Locate and identify every blood parasite.
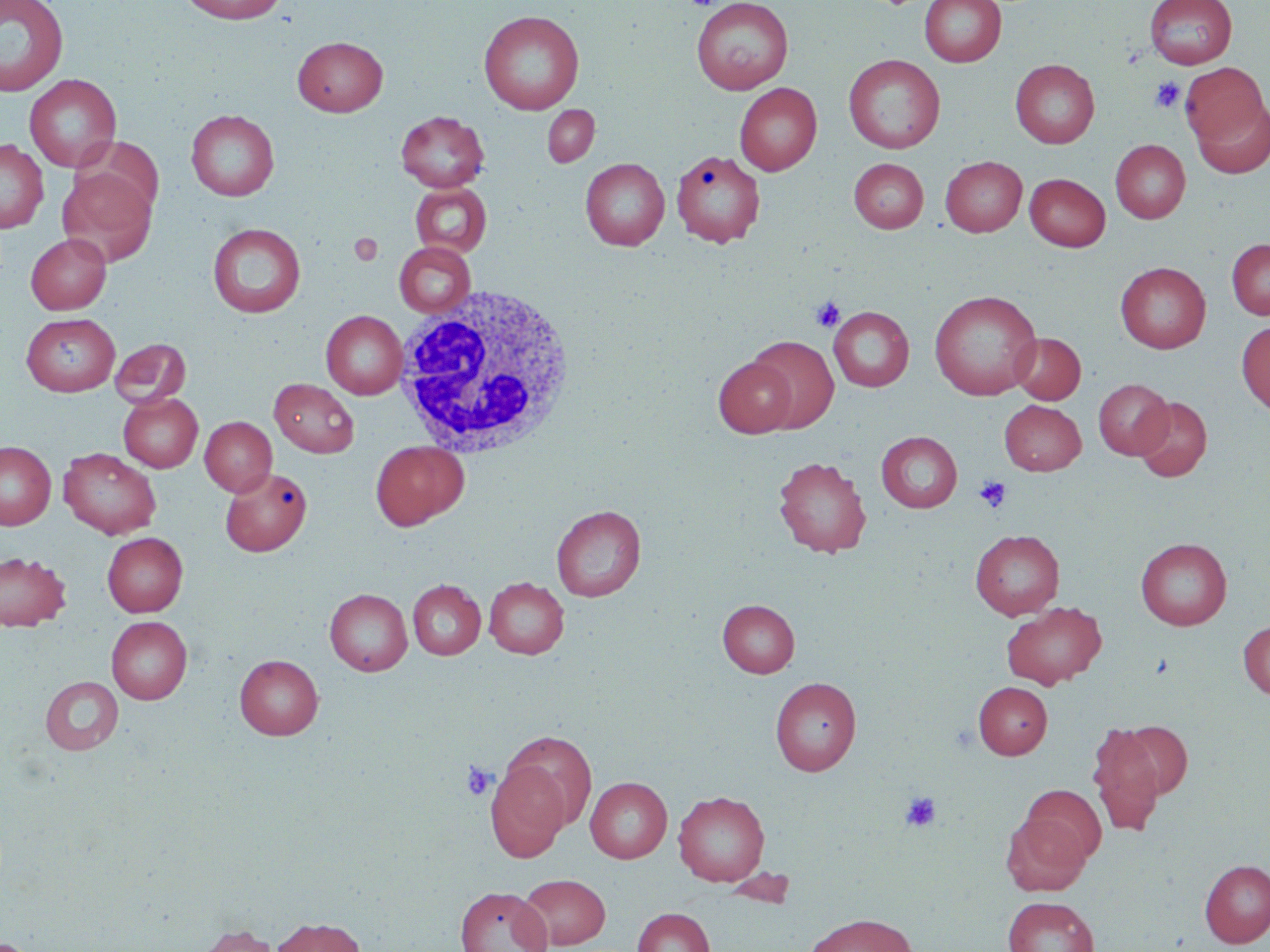

No blood parasites observed.

Approximate bounding boxes as named x1/y1/x2/y2 corners in pixels. White blood cell locations: (x1=389, y1=285, x2=580, y2=461). Uninfected red blood cell locations: (x1=0, y1=0, x2=69, y2=97), (x1=177, y1=0, x2=289, y2=24), (x1=691, y1=0, x2=793, y2=94), (x1=920, y1=0, x2=1006, y2=67), (x1=1145, y1=0, x2=1237, y2=69), (x1=479, y1=10, x2=585, y2=114), (x1=293, y1=36, x2=387, y2=116), (x1=844, y1=54, x2=945, y2=153), (x1=1010, y1=59, x2=1099, y2=148), (x1=1180, y1=63, x2=1268, y2=147), (x1=24, y1=74, x2=122, y2=173), (x1=735, y1=83, x2=822, y2=175), (x1=1191, y1=98, x2=1270, y2=178), (x1=542, y1=105, x2=599, y2=168), (x1=186, y1=109, x2=279, y2=200), (x1=396, y1=111, x2=489, y2=191), (x1=77, y1=137, x2=164, y2=218), (x1=0, y1=139, x2=49, y2=233), (x1=1110, y1=140, x2=1190, y2=223), (x1=671, y1=150, x2=765, y2=247), (x1=941, y1=156, x2=1026, y2=236), (x1=580, y1=158, x2=669, y2=251), (x1=849, y1=158, x2=928, y2=233), (x1=58, y1=168, x2=156, y2=267), (x1=1025, y1=174, x2=1110, y2=251), (x1=409, y1=183, x2=492, y2=257), (x1=208, y1=223, x2=306, y2=317), (x1=26, y1=233, x2=111, y2=314), (x1=1227, y1=239, x2=1270, y2=320), (x1=394, y1=241, x2=476, y2=317), (x1=1115, y1=262, x2=1211, y2=353), (x1=929, y1=290, x2=1042, y2=400), (x1=828, y1=307, x2=914, y2=391), (x1=321, y1=310, x2=407, y2=399), (x1=21, y1=313, x2=120, y2=396), (x1=1236, y1=320, x2=1270, y2=416), (x1=1010, y1=333, x2=1085, y2=404), (x1=747, y1=335, x2=839, y2=433), (x1=110, y1=338, x2=191, y2=408), (x1=714, y1=356, x2=797, y2=437), (x1=269, y1=378, x2=359, y2=457), (x1=1093, y1=379, x2=1173, y2=459), (x1=119, y1=393, x2=203, y2=472), (x1=1132, y1=396, x2=1212, y2=482), (x1=999, y1=400, x2=1086, y2=475), (x1=200, y1=416, x2=276, y2=495), (x1=876, y1=431, x2=962, y2=512), (x1=370, y1=440, x2=469, y2=530), (x1=0, y1=441, x2=56, y2=530), (x1=59, y1=448, x2=161, y2=539), (x1=773, y1=456, x2=871, y2=557), (x1=220, y1=466, x2=312, y2=556), (x1=551, y1=505, x2=646, y2=601), (x1=970, y1=529, x2=1064, y2=620), (x1=103, y1=533, x2=187, y2=617), (x1=1136, y1=538, x2=1232, y2=630), (x1=0, y1=551, x2=70, y2=631), (x1=484, y1=577, x2=569, y2=658), (x1=408, y1=580, x2=486, y2=659), (x1=325, y1=588, x2=413, y2=675), (x1=718, y1=599, x2=799, y2=677), (x1=1001, y1=600, x2=1106, y2=689), (x1=106, y1=616, x2=192, y2=703), (x1=1238, y1=621, x2=1270, y2=700), (x1=235, y1=654, x2=323, y2=739), (x1=40, y1=676, x2=123, y2=755), (x1=770, y1=677, x2=861, y2=775), (x1=974, y1=681, x2=1053, y2=759), (x1=1119, y1=720, x2=1193, y2=799), (x1=1087, y1=723, x2=1167, y2=836), (x1=500, y1=729, x2=599, y2=832), (x1=486, y1=760, x2=572, y2=860), (x1=585, y1=776, x2=672, y2=863), (x1=1020, y1=784, x2=1107, y2=866), (x1=673, y1=790, x2=770, y2=886), (x1=1002, y1=813, x2=1090, y2=895), (x1=1199, y1=859, x2=1270, y2=948), (x1=518, y1=873, x2=611, y2=949), (x1=455, y1=886, x2=552, y2=952), (x1=1003, y1=896, x2=1099, y2=952), (x1=632, y1=907, x2=714, y2=952), (x1=804, y1=913, x2=919, y2=952), (x1=271, y1=917, x2=366, y2=952), (x1=195, y1=924, x2=280, y2=952). Platelet locations: (x1=684, y1=0, x2=727, y2=9), (x1=1150, y1=77, x2=1185, y2=113), (x1=349, y1=233, x2=383, y2=265), (x1=811, y1=297, x2=845, y2=332), (x1=974, y1=475, x2=1011, y2=513), (x1=460, y1=761, x2=496, y2=800), (x1=900, y1=791, x2=942, y2=832). Slide-level diagnosis: negative for blood parasites. 1000x magnification. Single field of view. Thin blood smear. May-Grünwald-Giemsa-stained preparation. Image is 1270×952 pixels. Light microscopy.